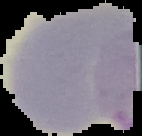 Malaria status: uninfected. The area outside the segmented cell region is set to black. Image is 142×136 pixels. From a thin blood film.